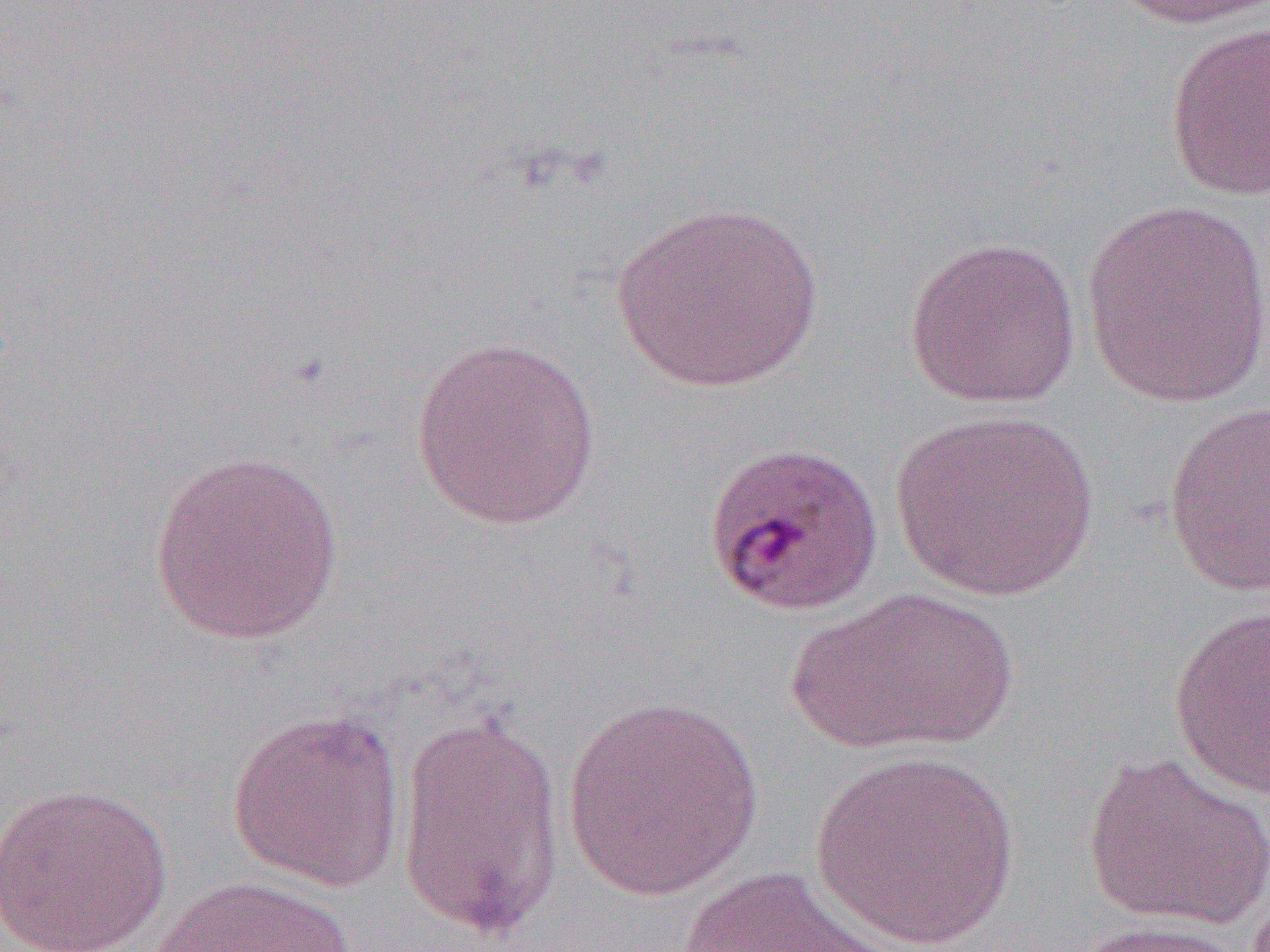
slide-level diagnosis = Plasmodium malariae
magnification = 1000x
uninfected red blood cell locations = approximate bounding boxes as (x1,y1)-(x2,y2) corner pairs in pixels: (1105,0)-(1269,30), (1164,19)-(1270,201), (1080,197)-(1270,409), (610,201)-(826,393), (903,236)-(1082,409), (408,336)-(602,531), (1162,401)-(1270,599), (887,409)-(1100,602), (149,450)-(344,646), (789,586)-(1017,755), (1169,604)-(1270,803), (560,694)-(764,903), (227,707)-(406,893), (394,708)-(564,943), (809,751)-(1020,951), (1082,752)-(1270,931), (0,782)-(172,952), (668,865)-(908,952), (148,875)-(357,952), (1065,919)-(1253,951)
image size = 1270×952 pixels
modality = optical microscopy
field of view = single
preparation = thin blood film